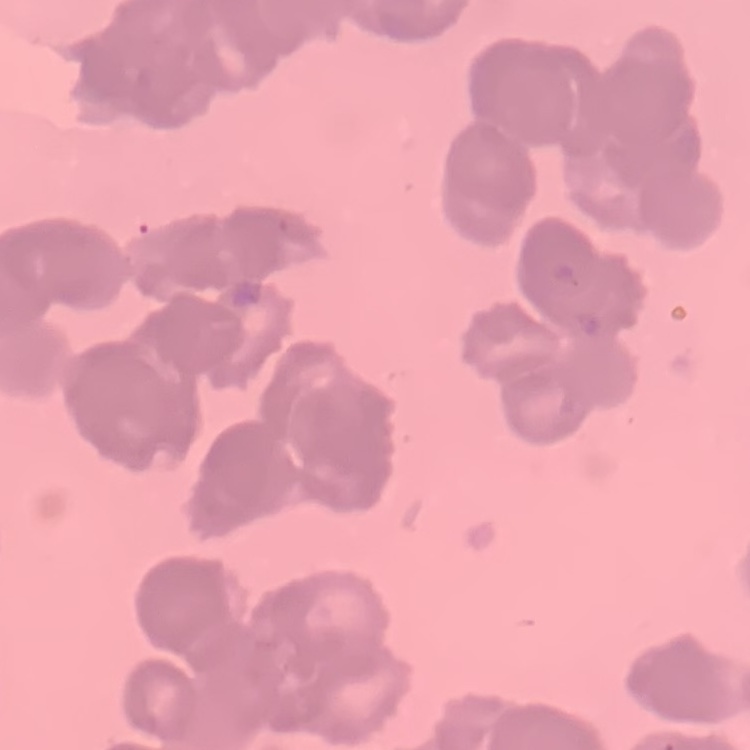
red blood cell morphology = rouleaux formation
image type = square crop of a larger photomicrograph
preparation = thin blood film
stain = Field's or Giemsa